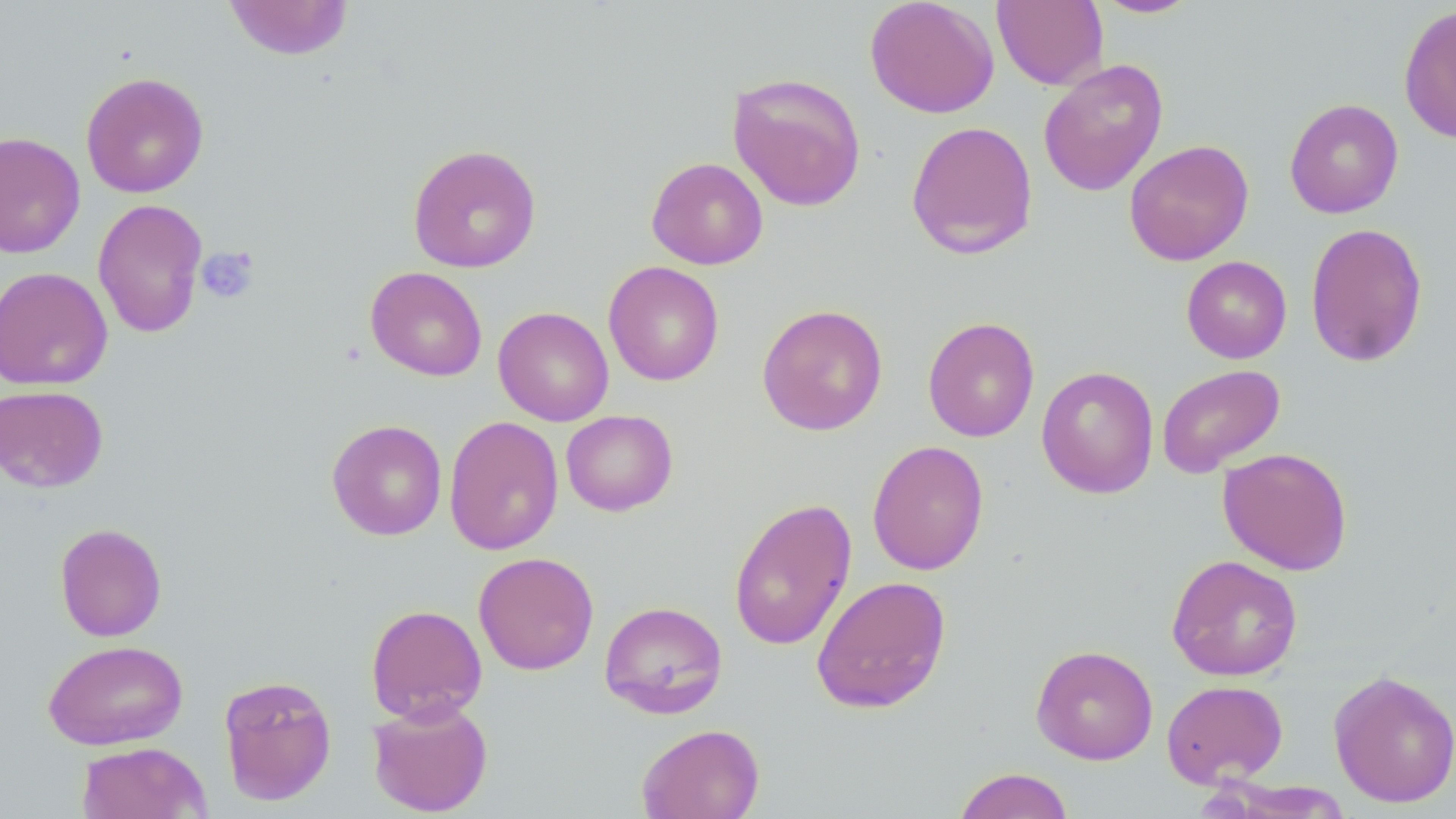
Summary:
  - Coordinate format: approximate bounding boxes as (x1, y1, x2, y2) in pixels
  - Platelet locations: (195, 246, 259, 304)
  - Uninfected red blood cell locations: (865, 0, 999, 118), (1091, 0, 1202, 19), (222, 1, 355, 61), (992, 1, 1108, 90), (1399, 4, 1456, 144), (1038, 59, 1168, 196), (80, 72, 209, 199), (727, 72, 867, 212), (1284, 98, 1403, 218), (906, 120, 1038, 260), (0, 131, 85, 260), (1124, 139, 1254, 266), (408, 143, 541, 273), (646, 157, 768, 270), (92, 198, 208, 339), (1305, 222, 1428, 367), (1181, 256, 1292, 363), (603, 261, 724, 386), (0, 266, 113, 391), (365, 266, 487, 381), (756, 303, 888, 436), (493, 306, 614, 426), (922, 316, 1040, 442), (1157, 364, 1285, 478), (1037, 366, 1159, 499), (0, 385, 108, 493), (561, 410, 678, 516), (444, 416, 563, 555), (327, 419, 447, 541), (867, 440, 989, 575), (1217, 447, 1353, 575), (728, 496, 857, 651), (54, 522, 167, 642), (473, 551, 599, 675), (1166, 555, 1303, 681), (811, 576, 951, 714), (599, 600, 728, 719), (365, 604, 488, 723), (43, 639, 189, 750), (1031, 645, 1158, 764), (1328, 670, 1456, 808), (218, 674, 338, 806), (1161, 679, 1288, 787), (367, 699, 493, 817), (636, 723, 765, 819), (76, 741, 212, 819), (953, 767, 1075, 819)
  - Slide-level diagnosis: negative for blood parasites
  - Field of view: single
  - Stain: May-Grünwald-Giemsa
  - Image size: 1456×819 pixels
  - Modality: light microscopy
  - Magnification: 1000x
  - Preparation: thin blood film